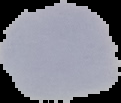

Summary:
  - Result: no malaria parasites detected
  - Image size: 121×103 pixels
  - Preparation: thin blood smear
  - Image type: segmented cell region with the area outside set to black